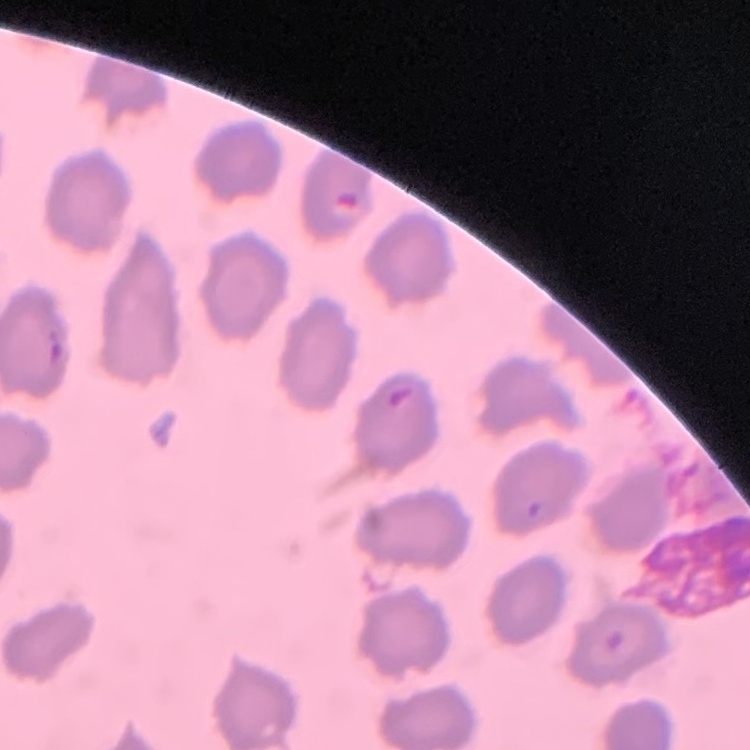
Summary:
  - Red blood cell morphology: no rouleaux formation
  - Stain: Field's or Giemsa
  - Preparation: thin blood smear
  - Image type: square crop of a larger photomicrograph